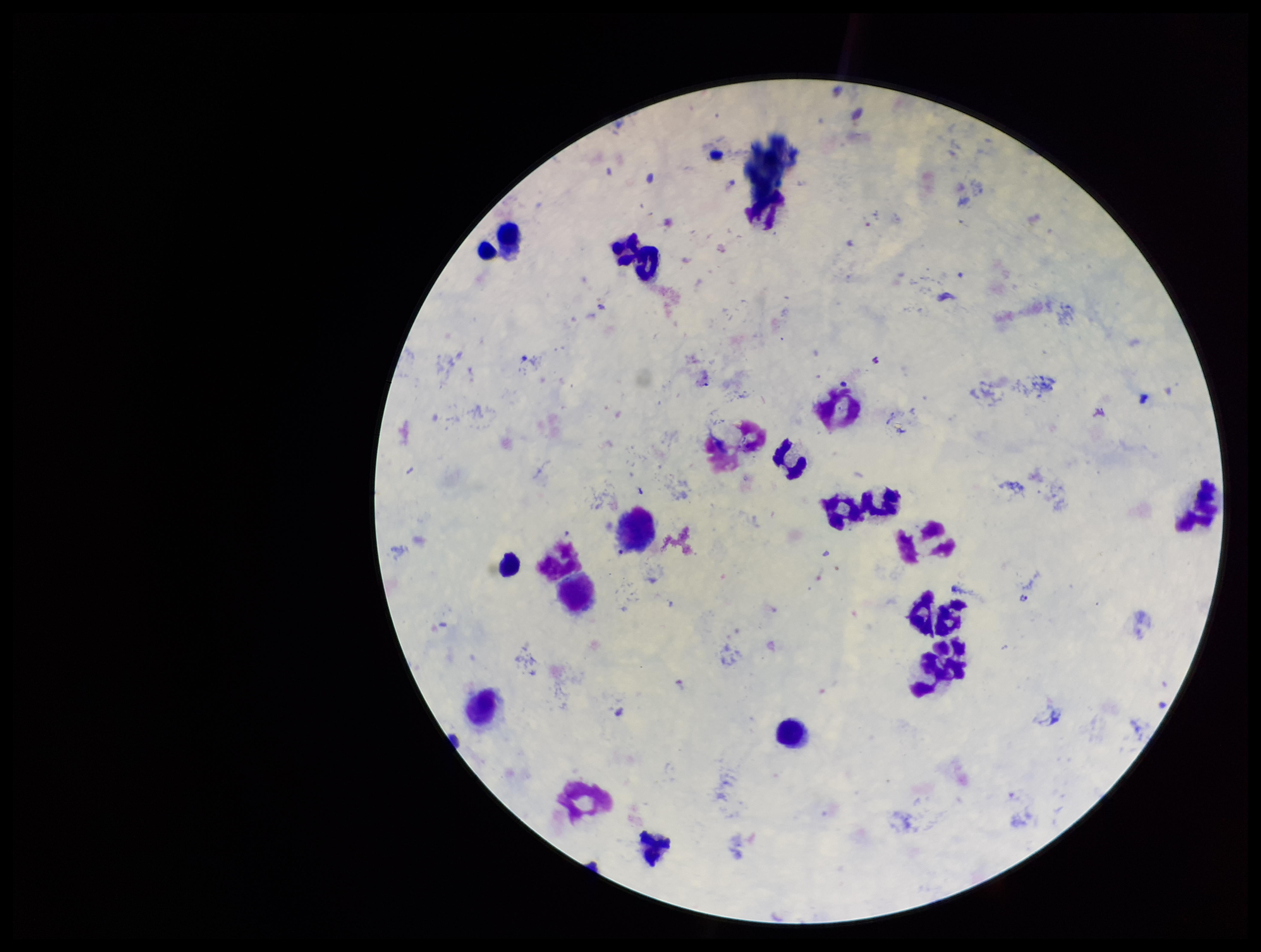

{
  "field_of_view": "one from this slide",
  "stain": "Giemsa",
  "plasmodium_parasites": "identified",
  "image_size": "1261×952 pixels",
  "parasite_count": 1,
  "capture": "smartphone photograph through the microscope eyepiece",
  "patient_malaria_status": "infected",
  "preparation": "thick blood smear",
  "species_reported_for_this_patient": "Plasmodium vivax",
  "leukocyte_count": 14
}